Locate every malaria parasite.
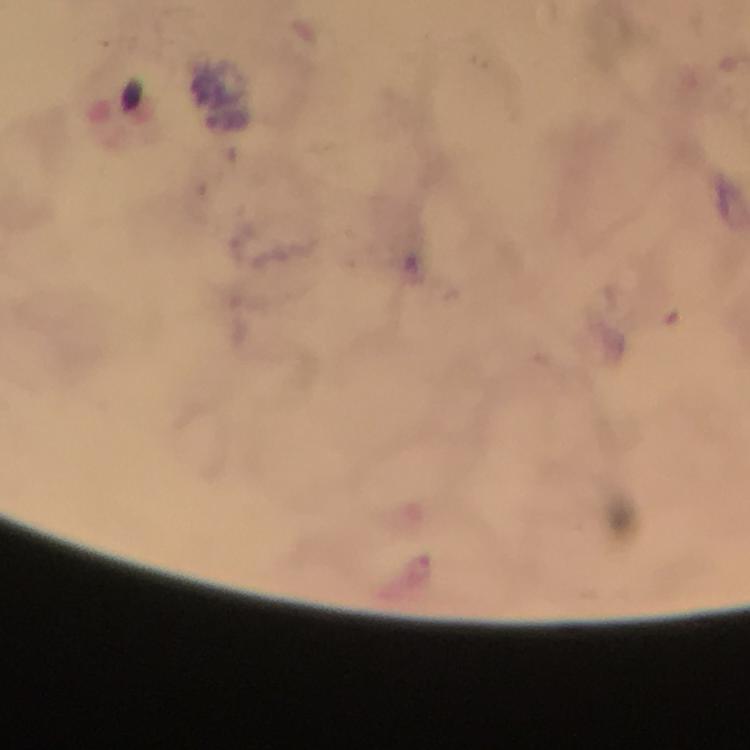
Approximate centers as [x, y] in pixels.
Malaria parasites: [419, 568].

Summary:
  - Magnification: 100x
  - Context: from a malaria diagnostic workup
  - Cropped from: a single field of view
  - Preparation: thick blood film
  - Immersion oil: applied
  - Image size: 750×750 pixels
  - Capture: smartphone photograph through a microscope
  - Stain: Giemsa